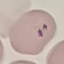
Result: malaria parasites identified. Photographed with a smartphone camera at the microscope eyepiece. Giemsa stain. Cell patch, automatically extracted from a larger field of view and resized to 64 × 64 pixels. Thin blood smear.